Assess this cell for malaria.
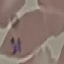
Parasitized.

preparation: thin smear
stain: Giemsa
image_type: cell patch, automatically extracted from a larger field of view and resized to 64 × 64 pixels
capture: smartphone through the microscope eyepiece